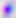
{
  "identification": "Toxoplasma gondii",
  "magnification": "400x",
  "modality": "micrograph"
}